Assess the morphology of the erythrocytes.
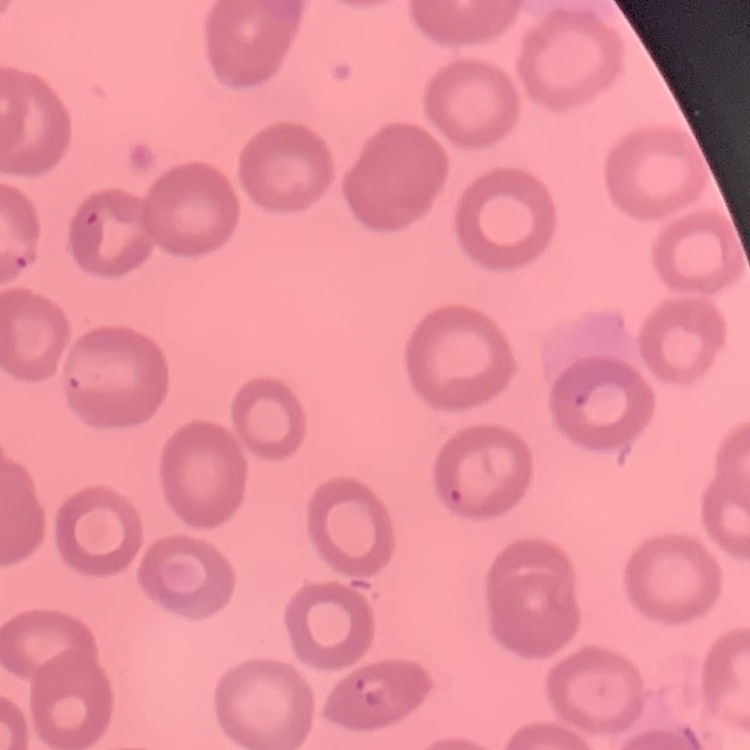

No rouleaux formation.

image_type: square crop of a larger photomicrograph
stain: Field's or Giemsa
preparation: thin peripheral smear